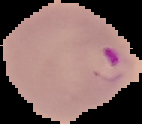 Image is 142×124 pixels. Result: Plasmodium parasites detected. From a thin blood film. Cell region segmented out of the field of view; the surrounding area is masked to black.